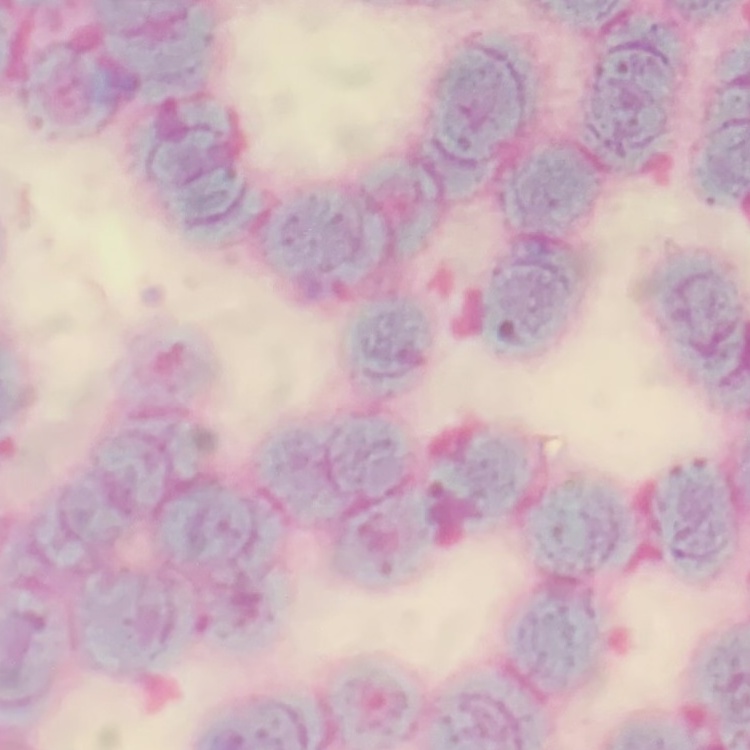
The erythrocytes show rouleaux formation. Thin blood film. One tile cut from a larger photomicrograph. Stained with either Field's or Giemsa.